Outline each Plasmodium ovale-infected red blood cell.
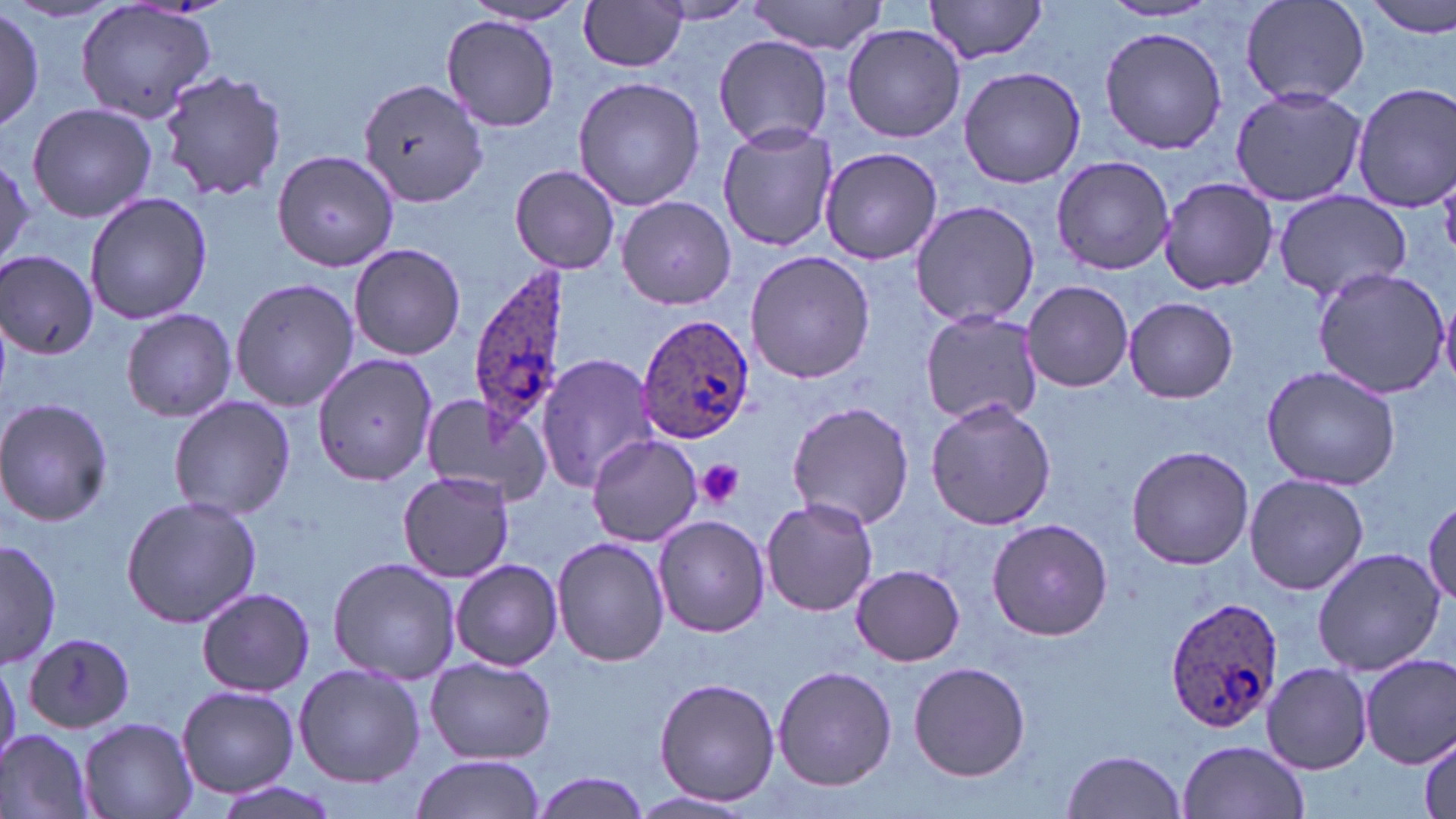

Approximate bounding boxes as named x1/y1/x2/y2 corners in pixels.
Plasmodium ovale-infected red blood cells: (x1=468, y1=263, x2=571, y2=450), (x1=638, y1=314, x2=755, y2=445), (x1=1164, y1=594, x2=1284, y2=733).

Summary:
  - Uninfected red blood cell locations: (x1=73, y1=0, x2=221, y2=125), (x1=1364, y1=0, x2=1456, y2=39), (x1=460, y1=1, x2=593, y2=29), (x1=578, y1=1, x2=689, y2=73), (x1=651, y1=1, x2=758, y2=26), (x1=746, y1=1, x2=887, y2=54), (x1=922, y1=1, x2=1051, y2=64), (x1=1240, y1=1, x2=1370, y2=108), (x1=1099, y1=2, x2=1222, y2=23), (x1=1, y1=9, x2=44, y2=129), (x1=441, y1=14, x2=561, y2=131), (x1=842, y1=23, x2=965, y2=143), (x1=1098, y1=25, x2=1227, y2=156), (x1=714, y1=35, x2=837, y2=148), (x1=957, y1=65, x2=1088, y2=188), (x1=157, y1=72, x2=289, y2=203), (x1=572, y1=75, x2=706, y2=212), (x1=358, y1=78, x2=487, y2=210), (x1=1350, y1=81, x2=1456, y2=211), (x1=1230, y1=85, x2=1366, y2=206), (x1=26, y1=101, x2=157, y2=225), (x1=718, y1=123, x2=840, y2=252), (x1=820, y1=145, x2=945, y2=265), (x1=273, y1=149, x2=401, y2=275), (x1=0, y1=152, x2=34, y2=270), (x1=1050, y1=155, x2=1175, y2=276), (x1=509, y1=163, x2=622, y2=275), (x1=1155, y1=176, x2=1280, y2=294), (x1=1270, y1=189, x2=1411, y2=304), (x1=83, y1=192, x2=214, y2=325), (x1=616, y1=196, x2=736, y2=309), (x1=908, y1=198, x2=1040, y2=329), (x1=349, y1=242, x2=466, y2=360), (x1=746, y1=251, x2=875, y2=384), (x1=1, y1=252, x2=100, y2=359), (x1=1311, y1=266, x2=1449, y2=397), (x1=230, y1=277, x2=360, y2=412), (x1=1022, y1=281, x2=1134, y2=392), (x1=1123, y1=296, x2=1238, y2=403), (x1=121, y1=308, x2=236, y2=422), (x1=918, y1=308, x2=1043, y2=427), (x1=537, y1=352, x2=661, y2=492), (x1=313, y1=357, x2=435, y2=486), (x1=1261, y1=364, x2=1400, y2=491), (x1=417, y1=391, x2=552, y2=509), (x1=168, y1=395, x2=296, y2=521), (x1=0, y1=397, x2=115, y2=528), (x1=924, y1=399, x2=1057, y2=533), (x1=785, y1=401, x2=915, y2=531), (x1=587, y1=432, x2=703, y2=548), (x1=1125, y1=444, x2=1254, y2=570), (x1=398, y1=469, x2=515, y2=582), (x1=1243, y1=472, x2=1369, y2=596), (x1=121, y1=495, x2=262, y2=627), (x1=1424, y1=495, x2=1456, y2=606), (x1=760, y1=497, x2=878, y2=616), (x1=653, y1=515, x2=769, y2=638), (x1=987, y1=517, x2=1112, y2=640), (x1=552, y1=536, x2=669, y2=667), (x1=1, y1=538, x2=59, y2=670), (x1=1311, y1=547, x2=1444, y2=676), (x1=326, y1=556, x2=460, y2=683), (x1=452, y1=558, x2=562, y2=672), (x1=852, y1=564, x2=963, y2=666), (x1=196, y1=586, x2=315, y2=697), (x1=23, y1=634, x2=137, y2=732), (x1=1362, y1=655, x2=1455, y2=770), (x1=426, y1=657, x2=556, y2=764), (x1=0, y1=660, x2=22, y2=766), (x1=909, y1=661, x2=1031, y2=782), (x1=293, y1=663, x2=425, y2=788), (x1=1261, y1=663, x2=1373, y2=774), (x1=773, y1=664, x2=896, y2=790), (x1=653, y1=676, x2=781, y2=807), (x1=176, y1=686, x2=300, y2=799), (x1=78, y1=716, x2=197, y2=819), (x1=0, y1=729, x2=94, y2=819), (x1=1417, y1=736, x2=1454, y2=819), (x1=1177, y1=740, x2=1310, y2=819), (x1=1061, y1=749, x2=1188, y2=819), (x1=409, y1=754, x2=548, y2=819), (x1=531, y1=771, x2=654, y2=818), (x1=205, y1=777, x2=343, y2=819), (x1=630, y1=790, x2=758, y2=816)
  - Platelet locations: (x1=696, y1=461, x2=746, y2=509)
  - Slide-level diagnosis: Plasmodium ovale
  - Preparation: thin blood smear
  - Image size: 1456×819 pixels
  - Magnification: 1000x
  - Modality: light microscopy
  - Field of view: one of a larger specimen
  - Stain: May-Grünwald-Giemsa